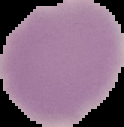

{
  "preparation": "thin blood film",
  "image_type": "segmented cell region on a black background",
  "image_size": "124×127 pixels",
  "malaria_status": "uninfected"
}